State which parasite is depicted.
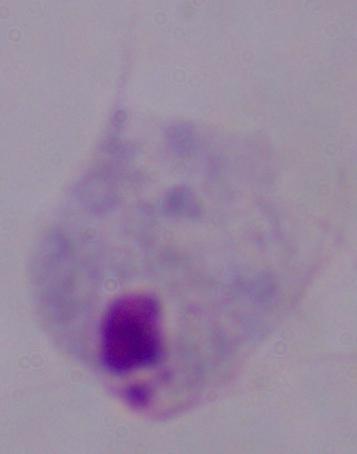

This is a trichomonad.

magnification: 1000x
modality: micrograph